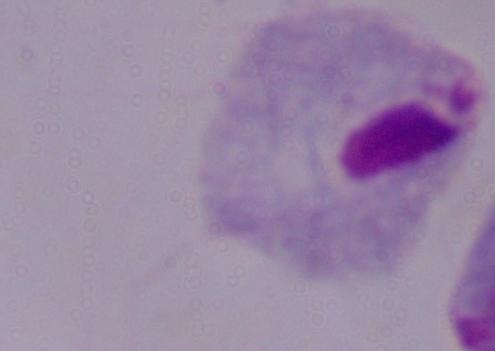
magnification = 1000x
modality = photomicrograph
identification = trichomonad